Assess the morphology of the red blood cells.
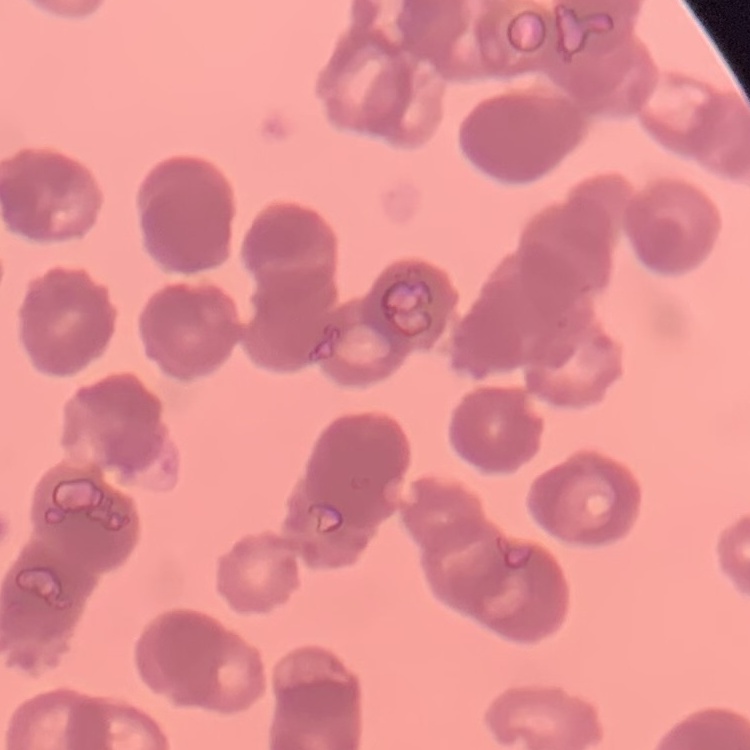

Rouleaux formation.

{
  "image_type": "one tile cut from a larger photomicrograph",
  "stain": "Field's or Giemsa",
  "preparation": "thin peripheral smear"
}